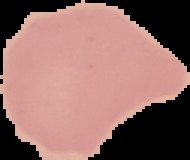

Summary:
  - Image size: 190×160 pixels
  - Result: no Plasmodium parasites seen
  - Image type: segmented cell region on a black background
  - Preparation: thin blood film